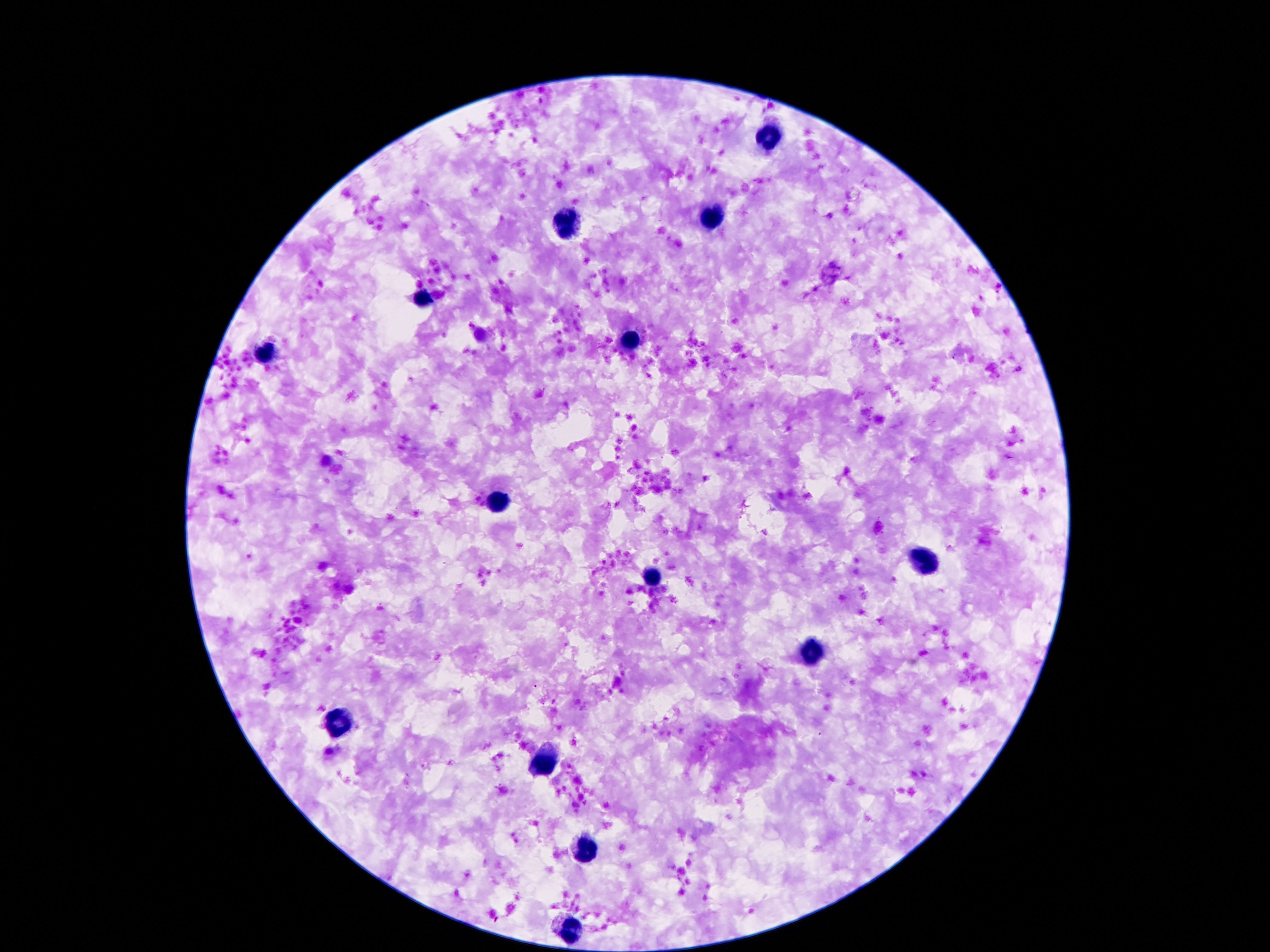
{
  "leukocyte_locations": "approximate centers as (x, y) in pixels: (769, 141), (710, 220), (567, 223), (423, 297), (633, 344), (267, 351), (500, 501), (923, 559), (653, 574), (809, 653), (344, 722), (547, 759), (586, 851), (571, 932)",
  "capture": "smartphone camera through the microscope eyepiece",
  "field_of_view": "one from this slide",
  "stain": "Giemsa",
  "magnification": "100x",
  "patient_malaria_status": "negative",
  "image_size": "1270×952 pixels",
  "preparation": "thick blood film"
}